Locate and identify every blood parasite.
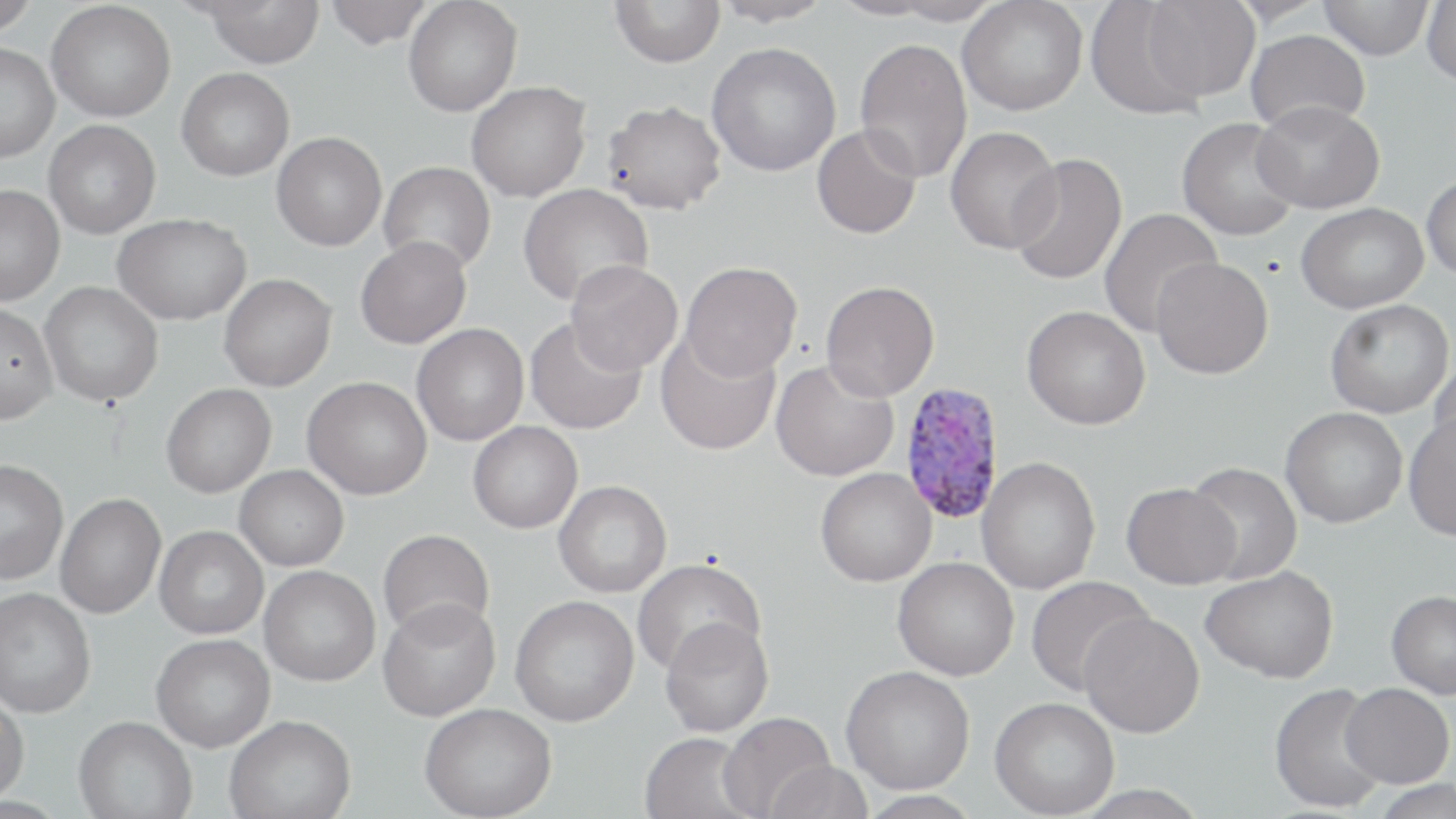
Approximate bounding boxes as named x1/y1/x2/y2 corners in pixels.
Plasmodium vivax-infected red blood cells: (x1=897, y1=382, x2=1006, y2=525).
No Plasmodium falciparum, Plasmodium ovale, Plasmodium malariae, Babesia divergens, or Trypanosoma brucei observed.

slide_level_diagnosis: Plasmodium vivax
magnification: 1000x
image_size: 1456×819 pixels
uninfected_red_blood_cell_locations: 'approximate bounding boxes as named x1/y1/x2/y2 corners in pixels: (x1=0, y1=0, x2=40, y2=35), (x1=197, y1=0, x2=325, y2=67), (x1=324, y1=0, x2=436, y2=49), (x1=403, y1=0, x2=522, y2=117), (x1=610, y1=0, x2=725, y2=68), (x1=711, y1=0, x2=835, y2=27), (x1=882, y1=0, x2=1004, y2=26), (x1=957, y1=0, x2=1088, y2=116), (x1=1141, y1=0, x2=1260, y2=102), (x1=1318, y1=0, x2=1434, y2=60), (x1=1421, y1=0, x2=1456, y2=87), (x1=46, y1=1, x2=176, y2=122), (x1=1085, y1=1, x2=1208, y2=118), (x1=1245, y1=29, x2=1370, y2=134), (x1=854, y1=38, x2=972, y2=182), (x1=706, y1=42, x2=841, y2=177), (x1=0, y1=43, x2=60, y2=162), (x1=176, y1=68, x2=294, y2=181), (x1=466, y1=81, x2=591, y2=202), (x1=601, y1=99, x2=727, y2=214), (x1=1252, y1=100, x2=1384, y2=214), (x1=1177, y1=118, x2=1301, y2=241), (x1=43, y1=120, x2=161, y2=238), (x1=811, y1=125, x2=922, y2=239), (x1=945, y1=126, x2=1062, y2=254), (x1=271, y1=132, x2=387, y2=251), (x1=1007, y1=153, x2=1127, y2=286), (x1=378, y1=161, x2=496, y2=275), (x1=1421, y1=174, x2=1456, y2=279), (x1=0, y1=184, x2=64, y2=305), (x1=517, y1=184, x2=653, y2=307), (x1=1296, y1=202, x2=1428, y2=313), (x1=1097, y1=208, x2=1223, y2=336), (x1=112, y1=213, x2=251, y2=325), (x1=355, y1=236, x2=472, y2=348), (x1=1150, y1=258, x2=1274, y2=379), (x1=564, y1=260, x2=682, y2=375), (x1=680, y1=261, x2=803, y2=380), (x1=219, y1=273, x2=337, y2=391), (x1=820, y1=280, x2=940, y2=400), (x1=39, y1=281, x2=163, y2=407), (x1=1324, y1=299, x2=1454, y2=419), (x1=0, y1=303, x2=58, y2=425), (x1=1021, y1=306, x2=1150, y2=430), (x1=524, y1=317, x2=648, y2=435), (x1=411, y1=323, x2=529, y2=446), (x1=654, y1=331, x2=780, y2=456), (x1=1430, y1=348, x2=1456, y2=465), (x1=771, y1=360, x2=899, y2=482), (x1=302, y1=376, x2=432, y2=500), (x1=161, y1=383, x2=276, y2=497), (x1=1280, y1=407, x2=1407, y2=528), (x1=1403, y1=414, x2=1456, y2=541), (x1=468, y1=421, x2=583, y2=533), (x1=976, y1=456, x2=1101, y2=594), (x1=0, y1=460, x2=69, y2=585), (x1=1184, y1=461, x2=1303, y2=585), (x1=235, y1=465, x2=349, y2=571), (x1=815, y1=468, x2=936, y2=587), (x1=553, y1=480, x2=672, y2=598), (x1=1121, y1=482, x2=1241, y2=589), (x1=55, y1=494, x2=165, y2=619), (x1=154, y1=526, x2=268, y2=639), (x1=377, y1=528, x2=495, y2=641), (x1=892, y1=557, x2=1019, y2=680), (x1=632, y1=558, x2=765, y2=676), (x1=259, y1=565, x2=381, y2=686), (x1=1200, y1=566, x2=1339, y2=683), (x1=1025, y1=575, x2=1153, y2=696), (x1=0, y1=587, x2=95, y2=718), (x1=1386, y1=590, x2=1456, y2=699), (x1=509, y1=595, x2=639, y2=726), (x1=378, y1=598, x2=501, y2=721), (x1=1079, y1=612, x2=1205, y2=737), (x1=659, y1=617, x2=774, y2=737), (x1=151, y1=634, x2=275, y2=752), (x1=841, y1=665, x2=975, y2=794), (x1=1269, y1=682, x2=1389, y2=813), (x1=1340, y1=683, x2=1454, y2=788), (x1=0, y1=691, x2=29, y2=804), (x1=989, y1=697, x2=1119, y2=818), (x1=419, y1=703, x2=557, y2=819), (x1=718, y1=712, x2=837, y2=819), (x1=224, y1=714, x2=357, y2=819), (x1=73, y1=716, x2=198, y2=819), (x1=639, y1=731, x2=757, y2=819), (x1=763, y1=760, x2=874, y2=819), (x1=1370, y1=778, x2=1456, y2=819), (x1=854, y1=790, x2=985, y2=818)'
field_of_view: one of a larger specimen
preparation: thin blood smear
modality: optical microscopy
stain: May-Grünwald-Giemsa